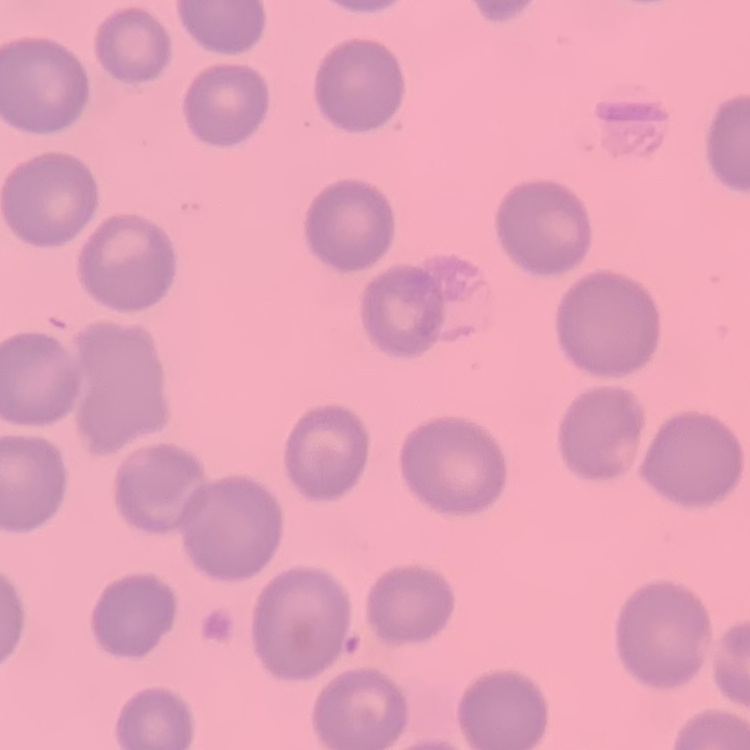
erythrocyte morphology = no rouleaux formation
preparation = thin blood film
image type = square crop of a larger photomicrograph
stain = Field's or Giemsa